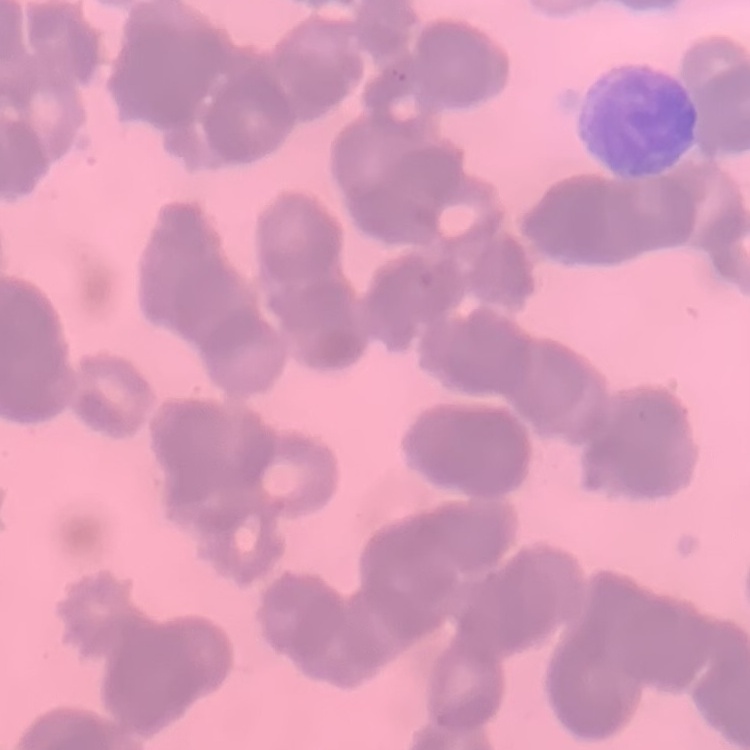

The erythrocytes show rouleaux formation. Field's or Giemsa stain. Square crop of a larger photomicrograph. Thin peripheral smear.